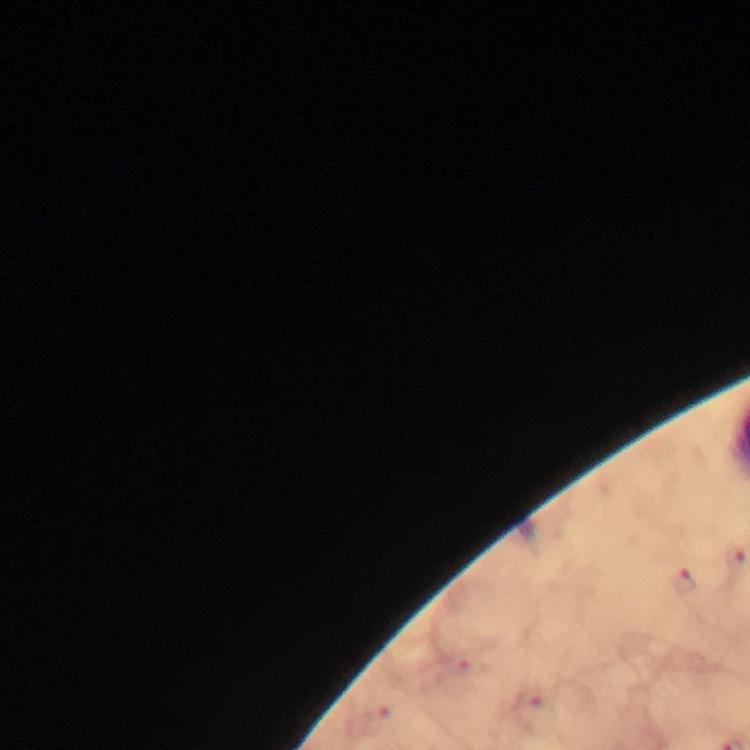
Approximate centers as [x, y] in pixels.
Summary:
  - Plasmodium parasite locations: [686, 582], [530, 698]
  - Magnification: 100x
  - Image size: 750×750 pixels
  - Cropped from: one field of view
  - Capture: smartphone mounted on the microscope
  - Context: from a diagnostic examination for malaria
  - Stain: Giemsa
  - Preparation: thick blood film
  - Immersion oil: applied